Locate every leukocyte (white blood cell).
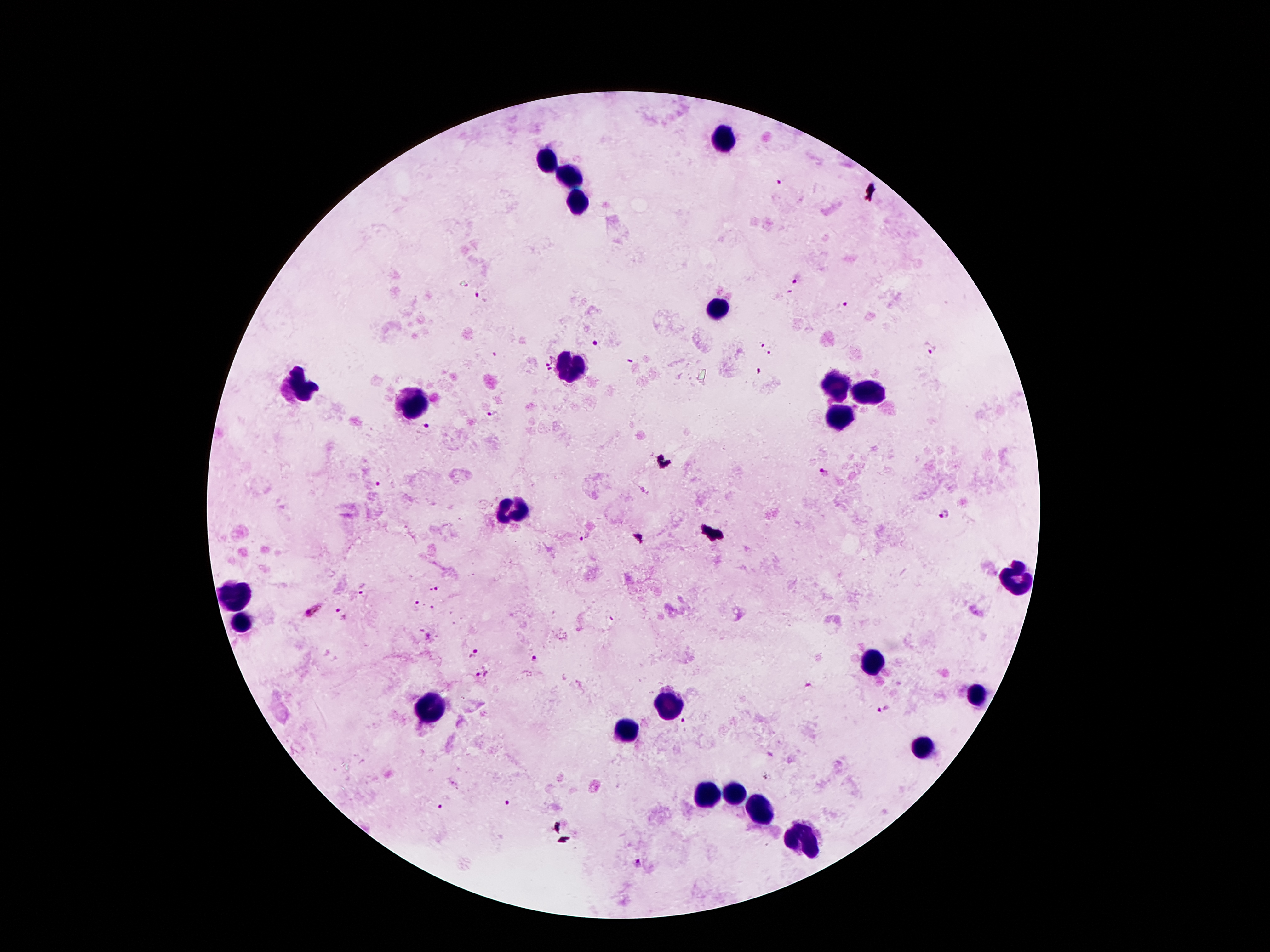

Approximate centers as (x, y) in pixels.
Leukocytes: (721, 139), (546, 160), (572, 180), (578, 201), (716, 307), (574, 363), (837, 383), (303, 388), (867, 393), (415, 402), (839, 421), (516, 510), (1014, 580), (233, 600), (242, 621), (872, 663), (975, 696), (672, 701), (431, 706), (632, 729), (924, 748), (707, 794), (735, 794), (760, 815), (804, 839).

{
  "field_of_view": "one from this slide",
  "stain": "Giemsa",
  "preparation": "thick peripheral-blood smear",
  "capture": "smartphone through the microscope eyepiece",
  "image_size": "1270×952 pixels",
  "magnification": "100x",
  "malaria_parasite_locations": "approximate centers as (x, y) in pixels: (780, 183), (796, 279), (478, 294), (846, 304), (594, 343), (760, 343), (930, 350), (769, 352), (547, 359), (629, 361), (550, 370), (494, 413), (427, 429), (824, 473), (376, 485), (942, 515), (583, 538), (435, 589), (365, 593), (416, 604), (312, 610), (341, 613), (474, 652), (534, 659), (481, 674), (809, 686), (886, 709), (683, 720), (506, 801), (439, 804), (635, 861)",
  "patient_malaria_status": "infected with Plasmodium falciparum"
}